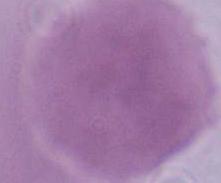

Summary:
  - Magnification: 1000x
  - Modality: photomicrograph
  - Identification: erythrocyte